Name the parasite shown.
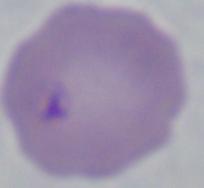

This is Babesia.

Captured at 1000x magnification. Micrograph.